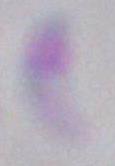

Summary:
  - Identification: Toxoplasma gondii
  - Modality: photomicrograph
  - Magnification: 1000x